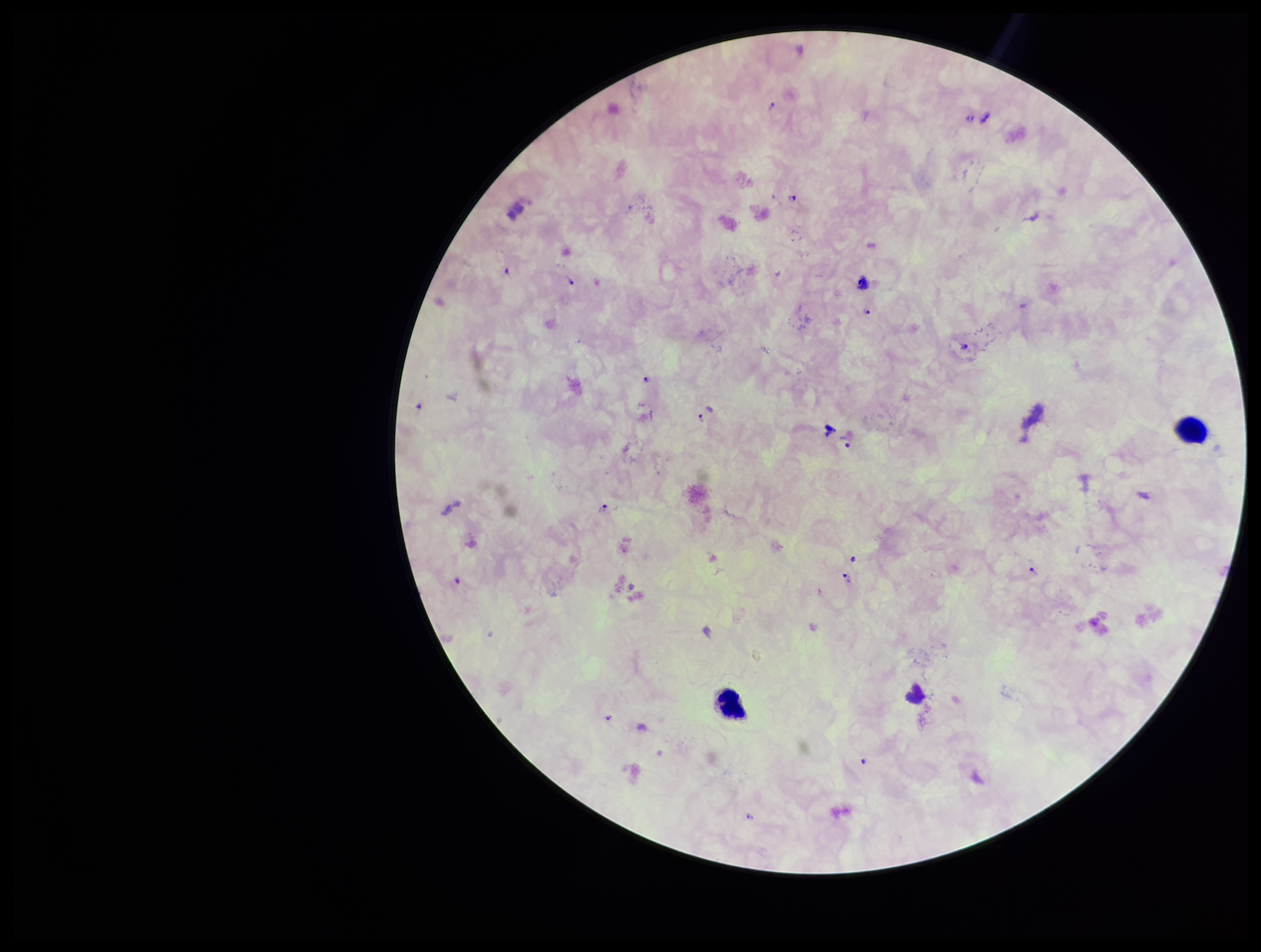
Summary:
  - Stain: Giemsa
  - Leukocyte count: 2
  - Patient malaria status: positive
  - Species reported for this patient: Plasmodium falciparum
  - Plasmodium parasites: detected
  - Capture: smartphone photograph through the microscope eyepiece
  - Preparation: thick blood smear
  - Image size: 1261×952 pixels
  - Field of view: single
  - Parasite count: 17